Give the extent of all uninfected red blood cells.
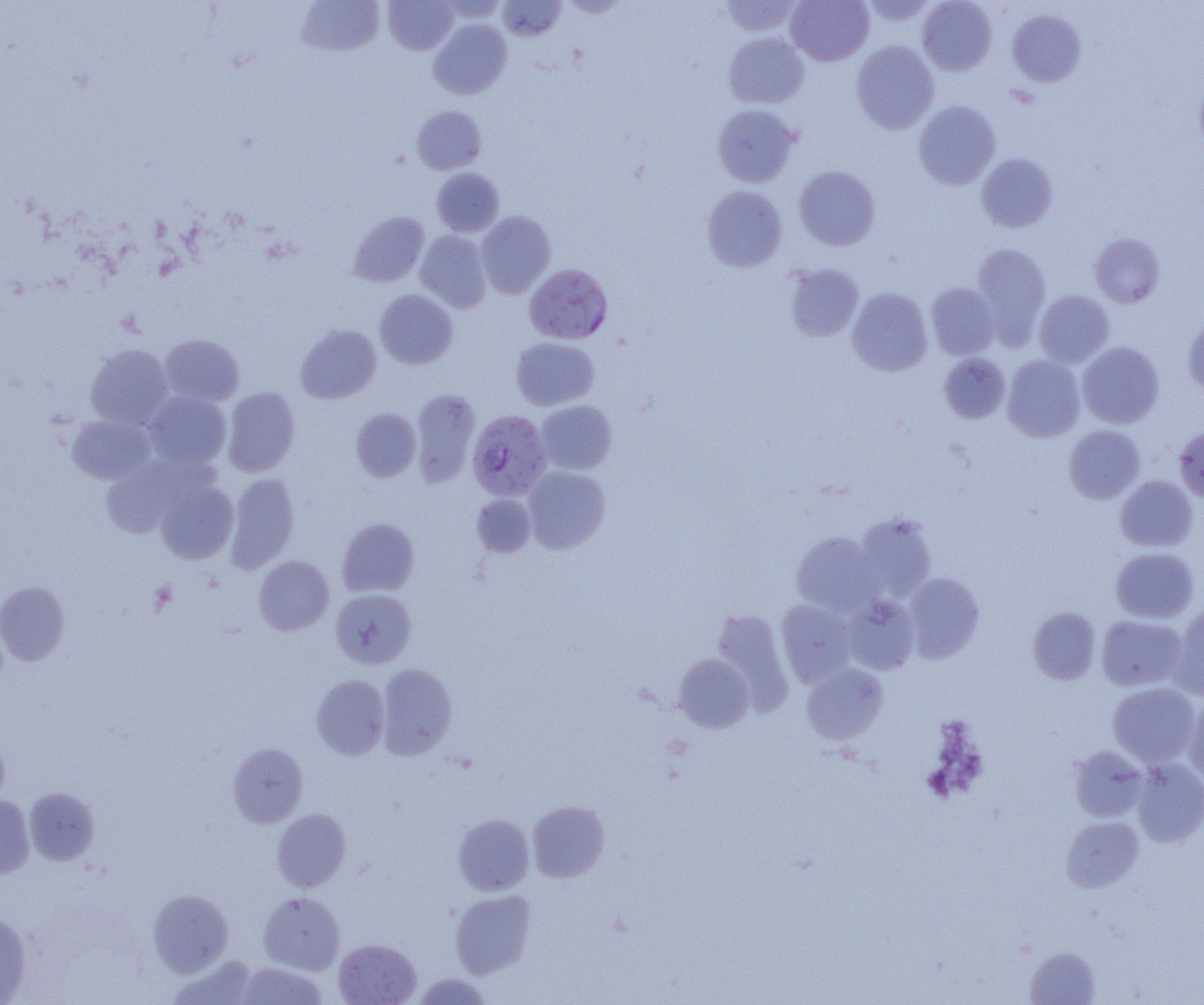
Approximate bounding boxes as [x1, y1, x2, y2] in pixels.
Uninfected red blood cells: [297, 0, 384, 56], [383, 0, 458, 55], [497, 0, 566, 41], [785, 0, 874, 66], [859, 0, 936, 26], [917, 0, 997, 75], [720, 1, 801, 37], [917, 4, 1086, 77], [1007, 9, 1086, 86], [428, 19, 512, 99], [723, 32, 809, 108], [851, 41, 939, 134], [914, 101, 1000, 189], [712, 104, 799, 187], [412, 105, 486, 175], [977, 153, 1058, 233], [794, 165, 880, 250], [431, 168, 504, 237], [702, 185, 787, 271], [348, 211, 429, 287], [476, 211, 555, 298], [415, 230, 492, 313], [1089, 233, 1165, 308], [971, 243, 1051, 345], [784, 262, 864, 342], [926, 282, 1000, 359], [847, 288, 933, 376], [375, 289, 457, 369], [1034, 290, 1114, 367], [1182, 315, 1204, 395], [296, 324, 381, 403], [160, 334, 244, 406], [511, 337, 599, 410], [1077, 342, 1164, 428], [86, 344, 173, 428], [939, 353, 1010, 423], [1002, 355, 1085, 442], [223, 387, 300, 476], [410, 388, 480, 488], [143, 391, 231, 470], [535, 400, 617, 475], [351, 408, 421, 482], [67, 414, 155, 484], [1174, 424, 1204, 502], [1063, 425, 1145, 504], [100, 455, 211, 537], [523, 466, 610, 553], [226, 473, 299, 574], [1115, 476, 1198, 552], [155, 480, 238, 564], [471, 493, 535, 557], [854, 512, 936, 601], [337, 518, 419, 597], [791, 531, 882, 616], [1110, 547, 1199, 623], [253, 555, 334, 635], [903, 572, 984, 663], [0, 582, 70, 665], [330, 589, 416, 669], [842, 595, 920, 675], [776, 600, 857, 687], [1170, 604, 1204, 701], [1027, 606, 1101, 685], [711, 609, 794, 714], [1096, 615, 1187, 691], [673, 654, 754, 732], [375, 663, 457, 759], [801, 663, 888, 745], [311, 674, 390, 759], [1108, 682, 1201, 766], [1183, 699, 1204, 788], [0, 730, 9, 807], [228, 742, 308, 827], [1067, 746, 1148, 822], [1131, 759, 1204, 849], [24, 787, 100, 866], [0, 794, 34, 879], [527, 801, 609, 882], [272, 808, 351, 892], [453, 814, 534, 895], [1061, 817, 1144, 892], [148, 889, 233, 976], [450, 890, 536, 978], [258, 891, 345, 974], [0, 911, 32, 1004], [334, 938, 421, 1005], [1025, 946, 1101, 1004], [168, 954, 259, 1005], [234, 961, 328, 1004], [412, 972, 492, 1004].

Summary:
  - Plasmodium falciparum-infected red blood cell locations: [524, 264, 613, 344], [467, 409, 552, 500]
  - Platelet locations: [149, 581, 177, 614]
  - Slide-level diagnosis: Plasmodium falciparum
  - Magnification: 1000x
  - Image size: 1204×1005 pixels
  - Preparation: thin blood smear
  - Modality: optical microscopy
  - Field of view: one of a larger specimen